Identify the blood parasite species.
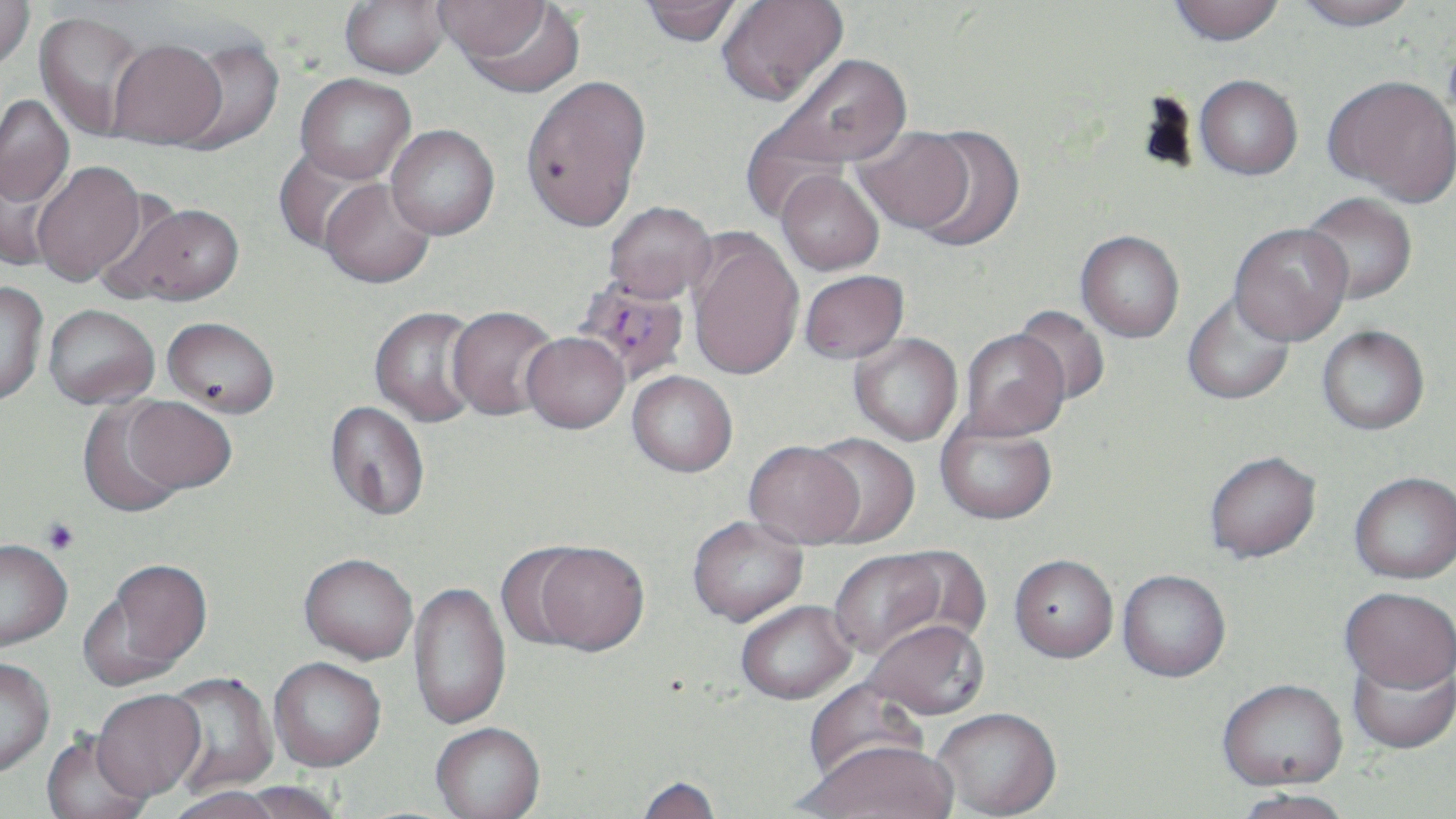

Plasmodium falciparum.

uninfected_red_blood_cell_locations: 'approximate bounding boxes as (x1, y1, x2, y2) in pixels: (0, 0, 35, 73), (339, 0, 450, 79), (717, 0, 848, 106), (1293, 0, 1420, 30), (434, 1, 551, 61), (638, 1, 745, 47), (1169, 1, 1285, 45), (456, 3, 586, 98), (34, 10, 150, 142), (168, 37, 285, 154), (107, 38, 228, 150), (764, 51, 913, 177), (295, 73, 415, 183), (520, 74, 652, 232), (1323, 74, 1456, 206), (1195, 75, 1303, 180), (0, 95, 75, 207), (386, 125, 499, 239), (854, 126, 974, 235), (910, 126, 1025, 250), (273, 148, 382, 256), (0, 159, 64, 273), (31, 160, 146, 286), (776, 169, 884, 276), (319, 178, 435, 288), (1301, 192, 1417, 305), (108, 201, 246, 306), (604, 201, 716, 303), (1229, 222, 1353, 346), (1076, 230, 1185, 342), (686, 231, 804, 381), (798, 269, 909, 364), (0, 280, 49, 408), (1181, 290, 1296, 406), (43, 304, 160, 410), (1013, 305, 1111, 406), (369, 306, 483, 427), (446, 306, 559, 421), (162, 316, 280, 419), (1317, 325, 1429, 436), (959, 328, 1070, 441), (521, 332, 628, 433), (849, 334, 963, 446), (627, 371, 738, 478), (123, 397, 236, 496), (77, 400, 190, 519), (324, 401, 430, 522), (935, 418, 1058, 526), (808, 434, 920, 549), (744, 442, 863, 550), (1205, 453, 1322, 565), (1349, 474, 1456, 587), (687, 518, 809, 629), (0, 538, 73, 651), (525, 545, 650, 659), (829, 550, 952, 662), (298, 555, 418, 666), (1008, 558, 1118, 666), (85, 559, 213, 686), (1117, 572, 1231, 685), (408, 582, 511, 732), (1340, 590, 1455, 698), (736, 603, 858, 708), (865, 623, 989, 724), (1348, 654, 1455, 756), (0, 658, 55, 777), (268, 659, 386, 775), (161, 672, 278, 796), (805, 676, 929, 787), (1218, 683, 1347, 794), (92, 691, 205, 804), (932, 711, 1062, 819), (431, 725, 545, 819), (40, 730, 153, 819), (802, 746, 956, 819), (635, 777, 722, 819), (236, 781, 344, 819), (168, 788, 283, 819), (1232, 792, 1355, 819)'
modality: light microscopy
image_size: 1456×819 pixels
stain: May-Grünwald-Giemsa
preparation: thin blood smear
magnification: 1000x
field_of_view: single
plasmodium_falciparum_infected_red_blood_cell_locations: 'approximate bounding boxes as (x1, y1, x2, y2) in pixels: (570, 275, 691, 385)'